Give the position of every Plasmodium parasite.
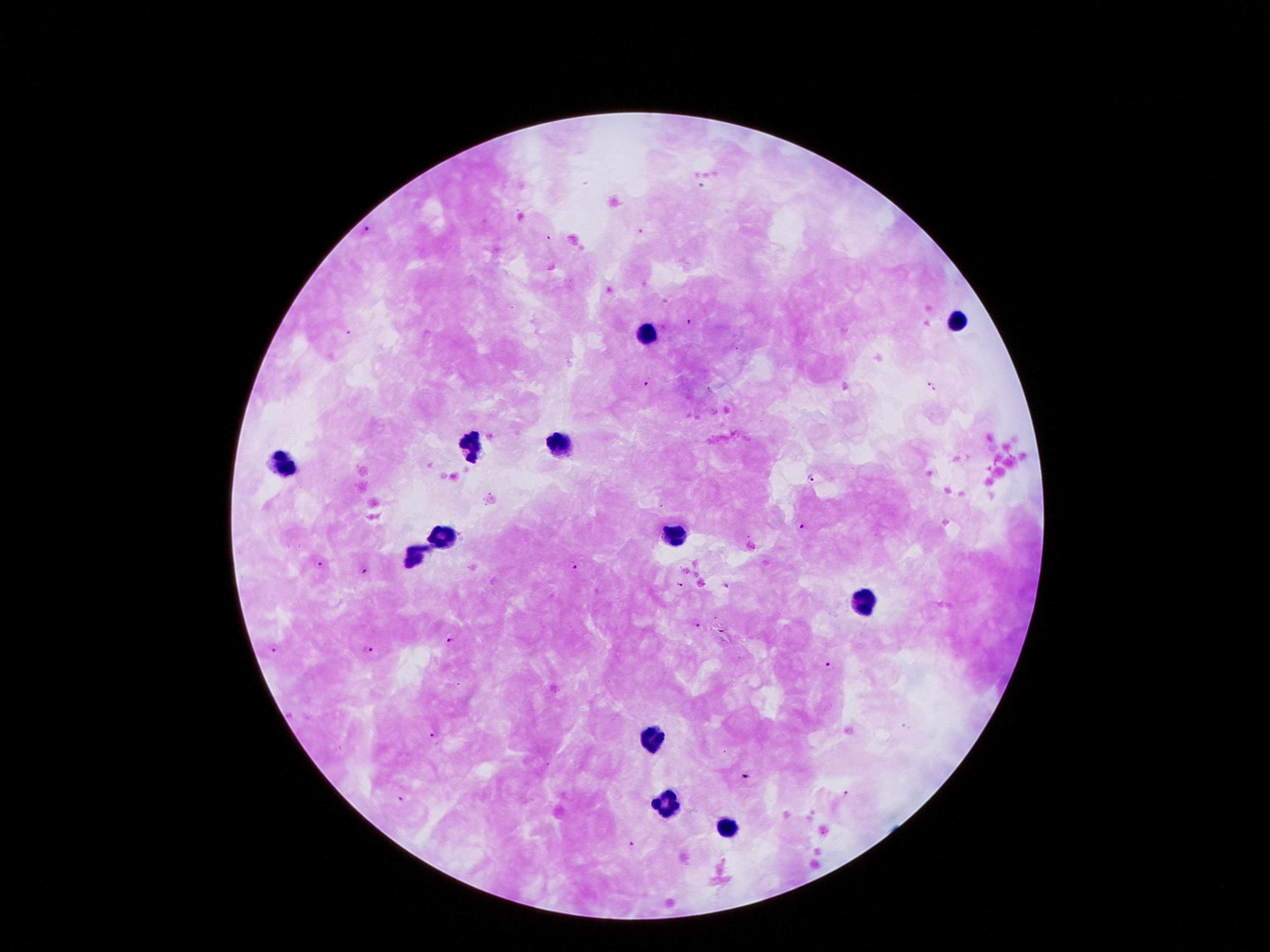
Approximate centers as [x, y] in pixels.
Plasmodium parasites: [366, 229], [641, 231], [551, 239], [687, 321], [647, 382], [931, 385], [812, 480], [802, 527], [319, 562], [572, 567], [365, 572], [680, 586], [698, 626], [722, 632], [451, 642], [274, 646], [367, 651], [828, 664], [435, 736], [745, 777], [849, 795], [401, 799], [632, 843].

Leukocyte locations: [961, 319], [643, 334], [561, 442], [470, 447], [287, 464], [678, 531], [444, 533], [416, 556], [862, 604], [653, 740], [668, 803], [729, 828]. Image is 1270×952 pixels. One field from this slide. Thick peripheral-blood smear. Smartphone photograph taken through the microscope eyepiece. 100x magnification. Giemsa-stained preparation. Patient malaria status: positive for Plasmodium falciparum.